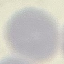

Summary:
  - Malaria status: uninfected
  - Stain: Giemsa
  - Preparation: thin smear
  - Image type: cell patch, automatically extracted from a larger field of view and resized to 64 × 64 pixels
  - Capture: smartphone through the microscope eyepiece